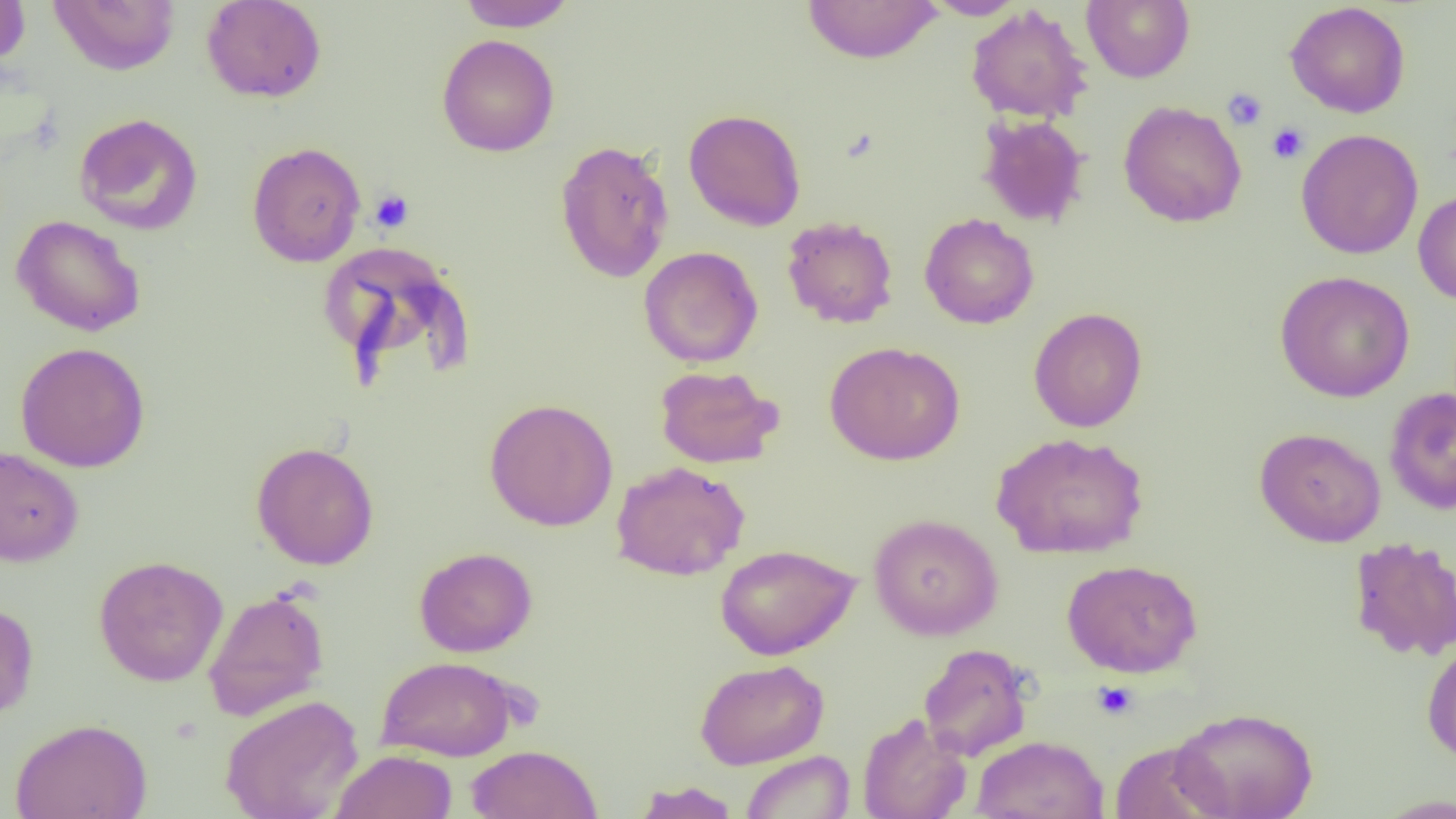
Summary:
  - Coordinate format: approximate bounding boxes as named x1/y1/x2/y2 corners in pixels
  - Uninfected red blood cell locations: (x1=0, y1=0, x2=30, y2=68), (x1=201, y1=0, x2=327, y2=103), (x1=457, y1=0, x2=575, y2=31), (x1=802, y1=0, x2=943, y2=64), (x1=921, y1=0, x2=1026, y2=20), (x1=1081, y1=0, x2=1195, y2=83), (x1=48, y1=1, x2=180, y2=75), (x1=1285, y1=1, x2=1411, y2=119), (x1=965, y1=5, x2=1093, y2=124), (x1=437, y1=34, x2=560, y2=157), (x1=1118, y1=100, x2=1247, y2=228), (x1=683, y1=109, x2=806, y2=232), (x1=74, y1=113, x2=203, y2=235), (x1=976, y1=114, x2=1090, y2=228), (x1=1296, y1=129, x2=1424, y2=259), (x1=554, y1=139, x2=675, y2=283), (x1=247, y1=141, x2=366, y2=267), (x1=1413, y1=189, x2=1456, y2=305), (x1=919, y1=213, x2=1039, y2=329), (x1=10, y1=214, x2=146, y2=337), (x1=782, y1=215, x2=899, y2=328), (x1=317, y1=239, x2=471, y2=378), (x1=639, y1=246, x2=763, y2=368), (x1=1275, y1=270, x2=1415, y2=402), (x1=1029, y1=307, x2=1148, y2=432), (x1=825, y1=341, x2=965, y2=465), (x1=14, y1=342, x2=150, y2=473), (x1=654, y1=364, x2=783, y2=469), (x1=1384, y1=387, x2=1456, y2=515), (x1=484, y1=398, x2=618, y2=531), (x1=1254, y1=427, x2=1386, y2=547), (x1=991, y1=432, x2=1149, y2=559), (x1=251, y1=442, x2=379, y2=569), (x1=0, y1=445, x2=84, y2=567), (x1=611, y1=461, x2=750, y2=580), (x1=869, y1=513, x2=1003, y2=640), (x1=1348, y1=535, x2=1456, y2=661), (x1=715, y1=543, x2=860, y2=660), (x1=414, y1=547, x2=537, y2=657), (x1=94, y1=555, x2=228, y2=687), (x1=1062, y1=559, x2=1202, y2=678), (x1=203, y1=587, x2=330, y2=721), (x1=0, y1=600, x2=38, y2=721), (x1=1421, y1=637, x2=1456, y2=765), (x1=918, y1=643, x2=1034, y2=761), (x1=375, y1=655, x2=519, y2=761), (x1=694, y1=658, x2=829, y2=769), (x1=221, y1=694, x2=364, y2=819), (x1=1170, y1=707, x2=1318, y2=818), (x1=857, y1=714, x2=972, y2=819), (x1=11, y1=717, x2=153, y2=819), (x1=971, y1=735, x2=1109, y2=819), (x1=1108, y1=740, x2=1227, y2=819), (x1=466, y1=744, x2=602, y2=818), (x1=331, y1=750, x2=457, y2=819), (x1=741, y1=750, x2=855, y2=818), (x1=633, y1=780, x2=741, y2=819), (x1=1373, y1=793, x2=1456, y2=818)
  - Platelet locations: (x1=1222, y1=88, x2=1267, y2=131), (x1=1266, y1=122, x2=1309, y2=164), (x1=369, y1=189, x2=414, y2=232), (x1=1092, y1=681, x2=1139, y2=720)
  - Slide-level diagnosis: no evidence of blood parasites
  - Image size: 1456×819 pixels
  - Preparation: thin blood film
  - Modality: light microscopy
  - Magnification: 1000x
  - Field of view: one of a larger specimen